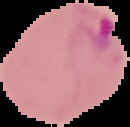

image size = 130×127 pixels
image type = cell region segmented out of the field of view; surrounding area masked to black
preparation = thin blood smear
result = Plasmodium parasites detected